Classify this cell by malaria status.
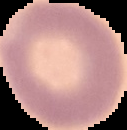
It is uninfected.

image type = cell region segmented out of the field of view; surrounding area masked to black
image size = 127×130 pixels
preparation = thin blood film